Outline each uninfected red blood cell.
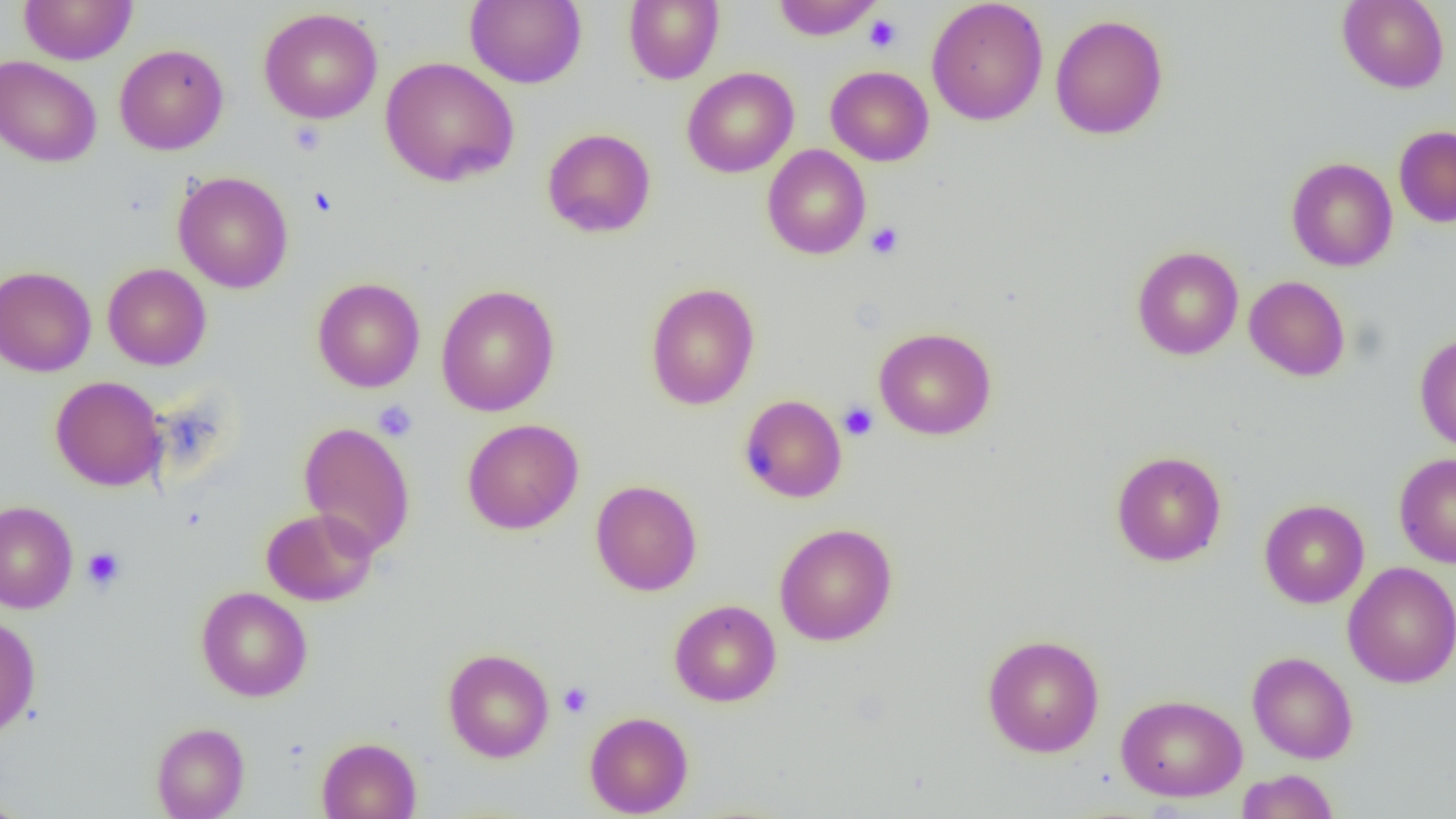

Approximate bounding boxes as (x1, y1, x2, y2) in pixels.
Uninfected red blood cells: (18, 0, 138, 65), (465, 0, 587, 88), (623, 0, 724, 84), (773, 0, 882, 40), (1337, 0, 1449, 92), (926, 1, 1049, 126), (259, 7, 382, 124), (1050, 14, 1168, 140), (114, 44, 228, 155), (0, 55, 101, 167), (380, 56, 519, 187), (825, 65, 934, 166), (682, 67, 799, 178), (1393, 126, 1456, 227), (542, 128, 656, 238), (762, 144, 871, 259), (1286, 157, 1398, 271), (172, 171, 293, 293), (1132, 246, 1244, 360), (102, 263, 211, 370), (0, 265, 97, 377), (1244, 275, 1350, 381), (312, 278, 425, 393), (645, 282, 760, 410), (435, 284, 559, 416), (874, 327, 997, 440), (1414, 332, 1456, 452), (50, 376, 166, 492), (739, 395, 847, 502), (462, 419, 584, 534), (298, 421, 416, 556), (1111, 450, 1227, 566), (1394, 452, 1456, 567), (590, 480, 702, 595), (1259, 499, 1369, 608), (0, 501, 78, 613), (261, 508, 378, 606), (775, 523, 897, 645), (1342, 561, 1456, 688), (196, 586, 312, 701), (669, 599, 781, 707), (0, 616, 40, 739), (981, 633, 1105, 757), (443, 648, 555, 762), (1247, 651, 1358, 764), (1116, 694, 1247, 802), (585, 711, 693, 818), (151, 722, 250, 819), (316, 737, 422, 819), (1237, 769, 1339, 819), (0, 795, 30, 819).

Platelet locations: (864, 14, 902, 53), (307, 186, 338, 216), (866, 222, 904, 260), (373, 401, 418, 442), (838, 402, 878, 440), (82, 547, 126, 591), (559, 682, 592, 717). Slide-level diagnosis: no evidence of blood parasites. One field of a larger specimen. 1000x magnification. Thin blood smear. Image is 1456×819 pixels. Light microscopy.